Name the blood parasite species.
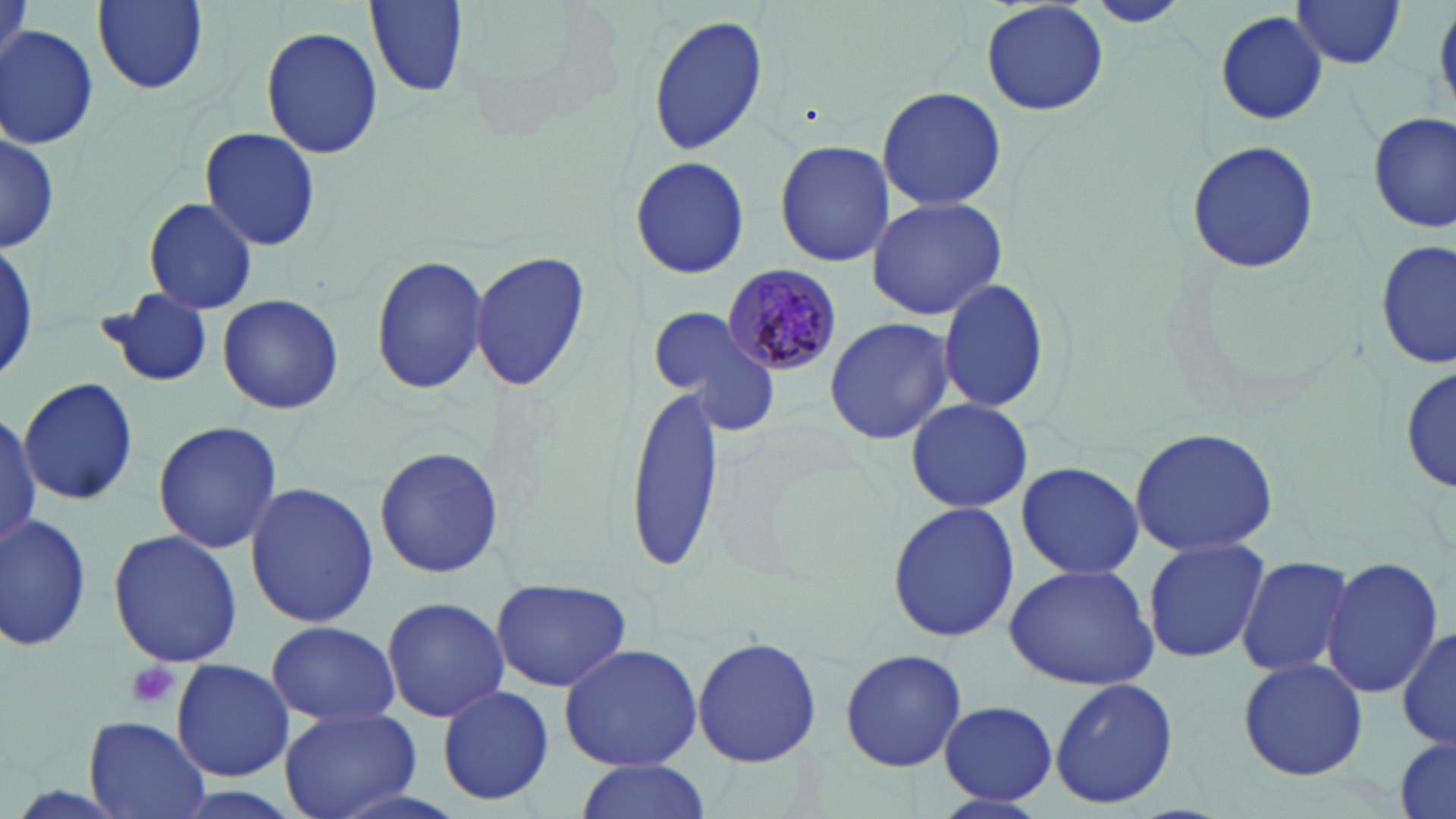

Plasmodium malariae.

Summary:
  - Coordinate format: approximate bounding boxes as (x1,y1)-(x2,y2) corner pairs in pixels
  - Plasmodium malariae-infected red blood cell locations: (722,262)-(844,374)
  - Platelet locations: (124,661)-(179,711)
  - Uninfected red blood cell locations: (93,0)-(208,94), (366,0)-(468,96), (1089,0)-(1187,26), (1291,0)-(1407,69), (981,1)-(1109,115), (1215,10)-(1328,126), (647,14)-(769,155), (261,23)-(382,159), (1,25)-(99,151), (875,86)-(1006,210), (1370,110)-(1454,233), (0,127)-(58,257), (199,128)-(321,251), (1187,137)-(1320,275), (774,138)-(895,268), (629,154)-(749,280), (866,195)-(1008,321), (142,196)-(260,316), (0,238)-(39,387), (1375,241)-(1455,369), (471,249)-(591,395), (370,254)-(489,396), (938,279)-(1050,413), (97,292)-(216,388), (217,293)-(344,415), (648,306)-(782,436), (824,316)-(954,446), (1402,363)-(1455,496), (19,377)-(140,505), (625,385)-(726,567), (905,398)-(1032,512), (0,411)-(42,546), (152,420)-(284,555), (1129,427)-(1281,557), (373,447)-(505,581), (1014,461)-(1147,579), (244,481)-(377,629), (885,499)-(1020,644), (0,512)-(93,653), (107,530)-(243,667), (1143,537)-(1270,665), (1235,554)-(1354,679), (1319,555)-(1443,697), (1003,564)-(1159,689), (489,577)-(632,692), (379,596)-(510,721), (265,620)-(402,728), (1396,625)-(1456,751), (692,636)-(823,768), (557,642)-(702,771), (839,649)-(968,771), (1238,656)-(1368,780), (171,658)-(295,782), (1050,677)-(1179,811), (436,685)-(557,808), (938,700)-(1059,804), (280,706)-(423,819), (83,715)-(208,819), (1393,735)-(1455,819), (572,757)-(712,819)
  - Stain: May-Grünwald-Giemsa
  - Field of view: single
  - Preparation: thin blood smear
  - Image size: 1456×819 pixels
  - Magnification: 1000x
  - Modality: light microscopy